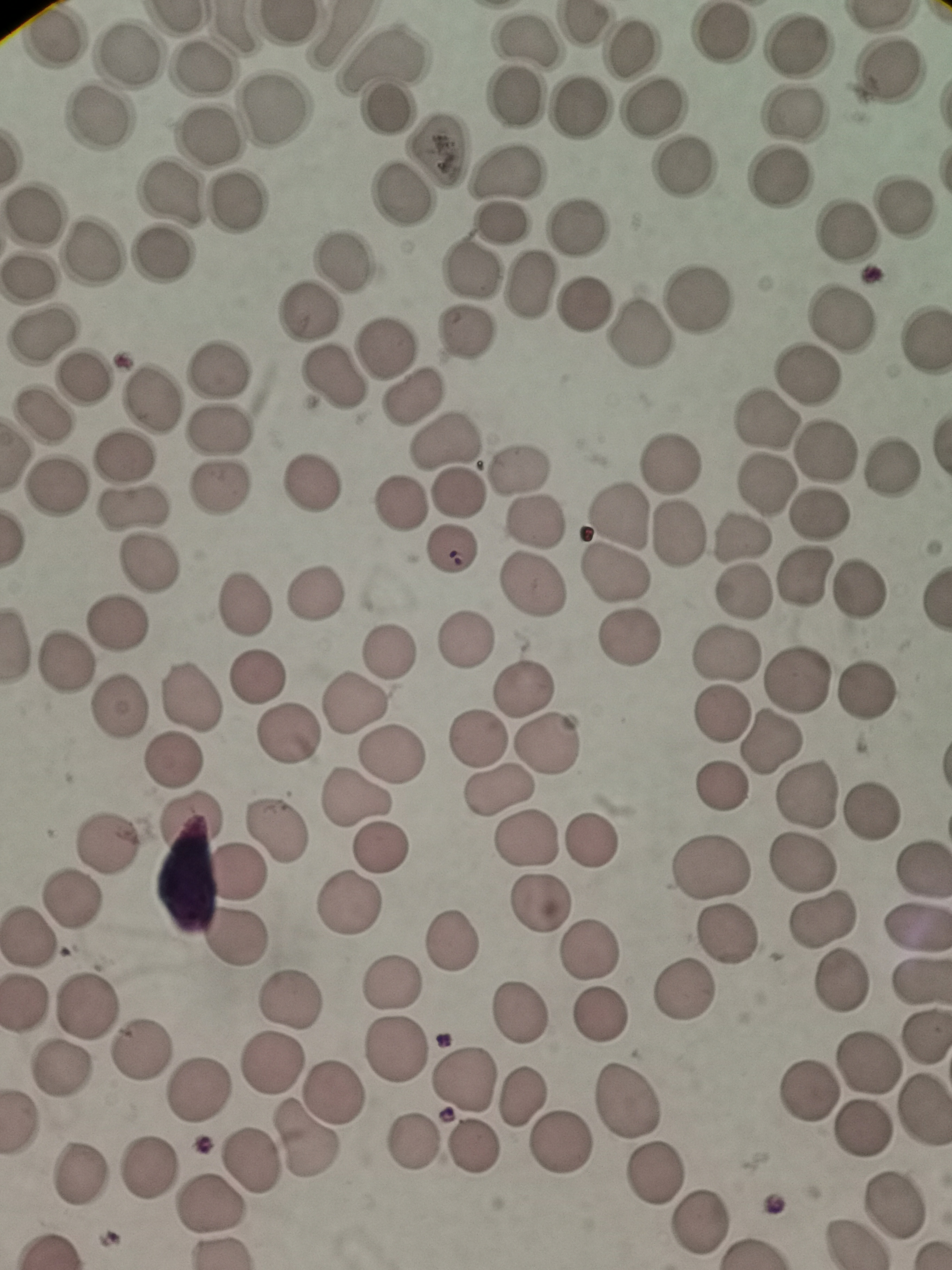

Approximate centers as [x, y] in pixels. Cell locations: [578, 25], [718, 33], [55, 39], [526, 39], [626, 47], [797, 47], [129, 55], [379, 61], [203, 67], [889, 70], [515, 92], [275, 108], [386, 108], [655, 108], [577, 111], [793, 114], [97, 122], [210, 136], [439, 148], [684, 167], [506, 173], [781, 178], [170, 194], [398, 198], [231, 207], [904, 208], [34, 213], [504, 221], [576, 224], [847, 230], [93, 252], [165, 257], [343, 261], [472, 269], [31, 281], [529, 285], [695, 298], [586, 301], [308, 311], [842, 318], [466, 331], [639, 332], [41, 334], [925, 336], [386, 349], [218, 368], [83, 376], [807, 379], [329, 380], [417, 397], [152, 401], [42, 414], [762, 420], [220, 429], [443, 443], [824, 452], [122, 459], [668, 462], [890, 467], [519, 472], [313, 483], [765, 485], [219, 486], [52, 488], [459, 496], [135, 504], [399, 505], [821, 514], [617, 517], [536, 521], [678, 533], [741, 536], [452, 552], [150, 563], [615, 576], [799, 579], [531, 585], [740, 590], [315, 591], [860, 592], [243, 605], [119, 621], [467, 639], [628, 639], [389, 652], [723, 655], [66, 661], [257, 677], [795, 679], [868, 689], [524, 691], [191, 698], [353, 703], [117, 704], [722, 715], [288, 733], [480, 739], [771, 740], [549, 743], [394, 753], [171, 763], [725, 790], [496, 792], [809, 797], [359, 799], [872, 813], [187, 818], [275, 829], [594, 840], [523, 841], [106, 843], [381, 846], [803, 864], [710, 867], [922, 867], [236, 873], [70, 899], [351, 902], [536, 905], [822, 919], [918, 927], [233, 935], [728, 938], [27, 939], [449, 942], [587, 949], [843, 978], [920, 981], [391, 984], [686, 992], [25, 1000], [294, 1001], [88, 1004], [522, 1012], [603, 1013], [927, 1041], [399, 1051], [136, 1054], [869, 1062], [269, 1066], [54, 1068], [461, 1080], [194, 1091], [332, 1092], [801, 1092], [522, 1097], [625, 1101], [924, 1114], [864, 1130], [305, 1136], [416, 1142], [562, 1142], [474, 1148], [251, 1162], [149, 1169], [80, 1172], [655, 1174], [208, 1203], [894, 1204], [696, 1223], [856, 1243]. Giemsa stain. One field from this slide. Photographed with a smartphone camera at the microscope eyepiece. Thin blood film. Image is 952×1270 pixels.